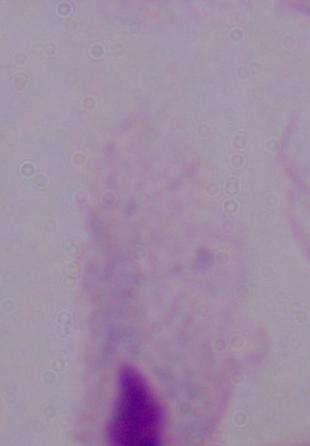
A trichomonad is seen. Captured at 1000x magnification. Micrograph.